Name the cell type shown.
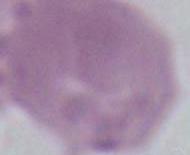
An erythrocyte.

Micrograph. Captured at 1000x magnification.